Locate every malaria parasite.
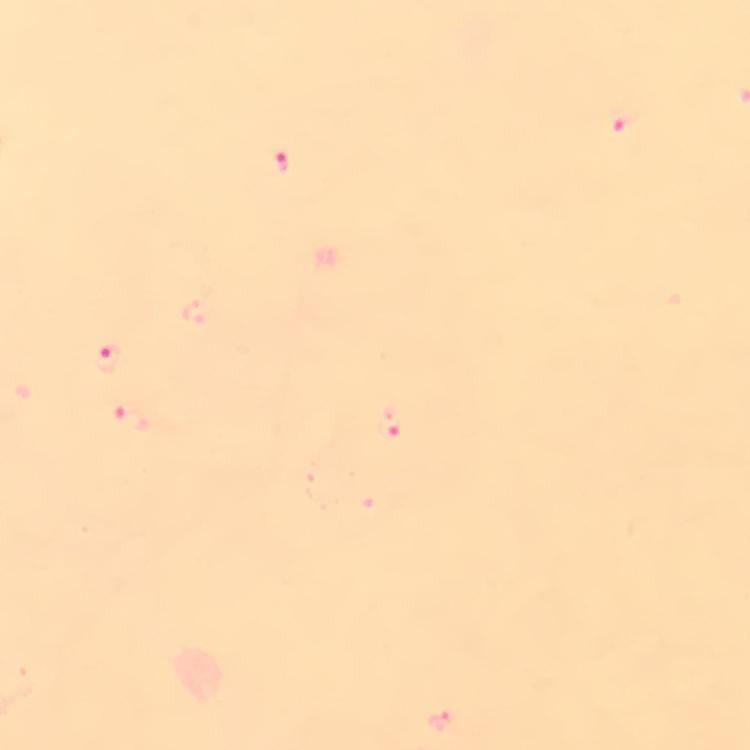

Approximate centers as (x, y) in pixels.
Malaria parasites: (621, 116), (281, 160), (110, 358), (131, 416), (390, 420), (441, 721).

{
  "preparation": "thick blood smear",
  "context": "from a malaria diagnostic workup",
  "stain": "Giemsa",
  "capture": "smartphone photograph through a microscope",
  "cropped_from": "a single field of view",
  "image_size": "750×750 pixels",
  "immersion_oil": "applied",
  "magnification": "100x"
}